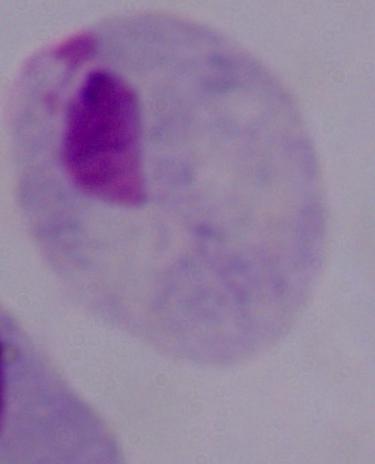
magnification: 1000x
modality: micrograph
identification: trichomonad